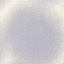
malaria_status: uninfected
capture: smartphone camera at the microscope eyepiece
preparation: thin blood film
stain: Giemsa
image_type: cell patch, automatically extracted from a larger field of view and resized to 64 × 64 pixels